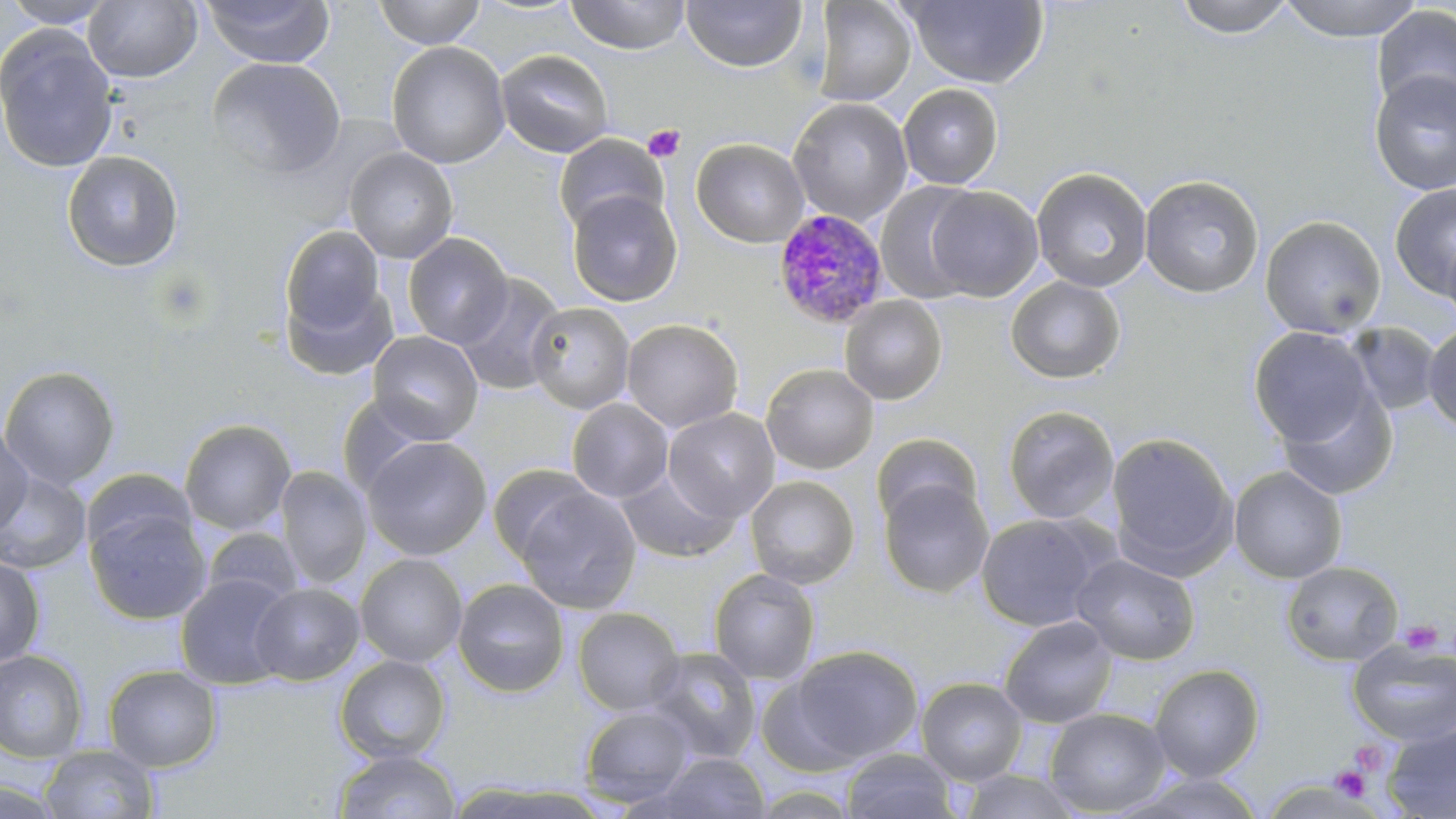

{
  "slide_level_diagnosis": "Plasmodium malariae",
  "uninfected_red_blood_cell_locations": "approximate bounding boxes as [x1, y1, x2, y2] in pixels: [0, 0, 117, 28], [201, 0, 334, 68], [374, 0, 485, 49], [565, 0, 691, 54], [681, 0, 807, 72], [1173, 0, 1297, 39], [1278, 0, 1426, 42], [83, 1, 202, 83], [811, 1, 916, 106], [905, 1, 1049, 87], [1372, 5, 1456, 116], [1, 25, 119, 174], [387, 41, 510, 169], [495, 49, 614, 158], [206, 56, 346, 178], [1369, 70, 1456, 196], [897, 83, 1004, 189], [788, 97, 913, 226], [553, 134, 668, 234], [691, 138, 809, 248], [344, 147, 458, 264], [61, 151, 184, 273], [1032, 167, 1152, 293], [1140, 174, 1265, 298], [874, 183, 982, 303], [1390, 183, 1456, 301], [925, 185, 1044, 301], [566, 190, 682, 307], [1260, 215, 1386, 338], [279, 225, 388, 343], [1441, 230, 1456, 327], [402, 232, 513, 349], [454, 272, 566, 396], [282, 275, 398, 382], [1006, 276, 1126, 384], [839, 295, 948, 405], [525, 302, 636, 414], [621, 318, 743, 432], [1346, 322, 1442, 415], [1422, 324, 1456, 433], [1247, 326, 1377, 448], [367, 330, 483, 443], [761, 363, 879, 474], [0, 365, 120, 490], [1276, 384, 1398, 501], [336, 394, 442, 496], [567, 398, 673, 502], [1002, 405, 1120, 524], [663, 408, 780, 521], [179, 418, 297, 536], [0, 425, 33, 536], [870, 432, 983, 531], [1106, 432, 1238, 577], [361, 435, 492, 561], [487, 463, 599, 565], [1228, 465, 1347, 583], [274, 466, 372, 589], [80, 467, 198, 560], [615, 467, 741, 563], [0, 471, 92, 574], [744, 475, 860, 589], [878, 478, 993, 598], [515, 487, 641, 614], [85, 505, 210, 625], [975, 512, 1111, 631], [202, 527, 306, 608], [355, 553, 468, 668], [1071, 554, 1200, 665], [0, 555, 45, 669], [1281, 560, 1404, 666], [709, 568, 820, 684], [175, 572, 295, 689], [453, 578, 570, 698], [249, 582, 364, 685], [572, 607, 684, 715], [998, 615, 1118, 728], [1347, 641, 1456, 747], [787, 645, 923, 765], [644, 646, 762, 762], [0, 649, 89, 762], [335, 655, 452, 763], [103, 664, 222, 772], [1149, 664, 1264, 782], [755, 672, 866, 776], [916, 677, 1028, 784], [579, 704, 696, 807], [1044, 708, 1171, 816], [1383, 722, 1455, 818], [38, 744, 160, 818], [332, 749, 462, 819], [841, 749, 958, 819], [652, 752, 771, 818], [955, 770, 1087, 818], [0, 778, 69, 819]",
  "stain": "May-Grünwald-Giemsa",
  "modality": "light microscopy",
  "platelet_locations": "approximate bounding boxes as [x1, y1, x2, y2] in pixels: [643, 125, 685, 162], [151, 266, 216, 332], [1399, 620, 1442, 656], [1348, 740, 1389, 776], [1331, 767, 1371, 801]",
  "magnification": "1000x",
  "field_of_view": "single",
  "image_size": "1456×819 pixels",
  "preparation": "thin blood film",
  "plasmodium_malariae_infected_red_blood_cell_locations": "approximate bounding boxes as [x1, y1, x2, y2] in pixels: [773, 209, 889, 328]"
}